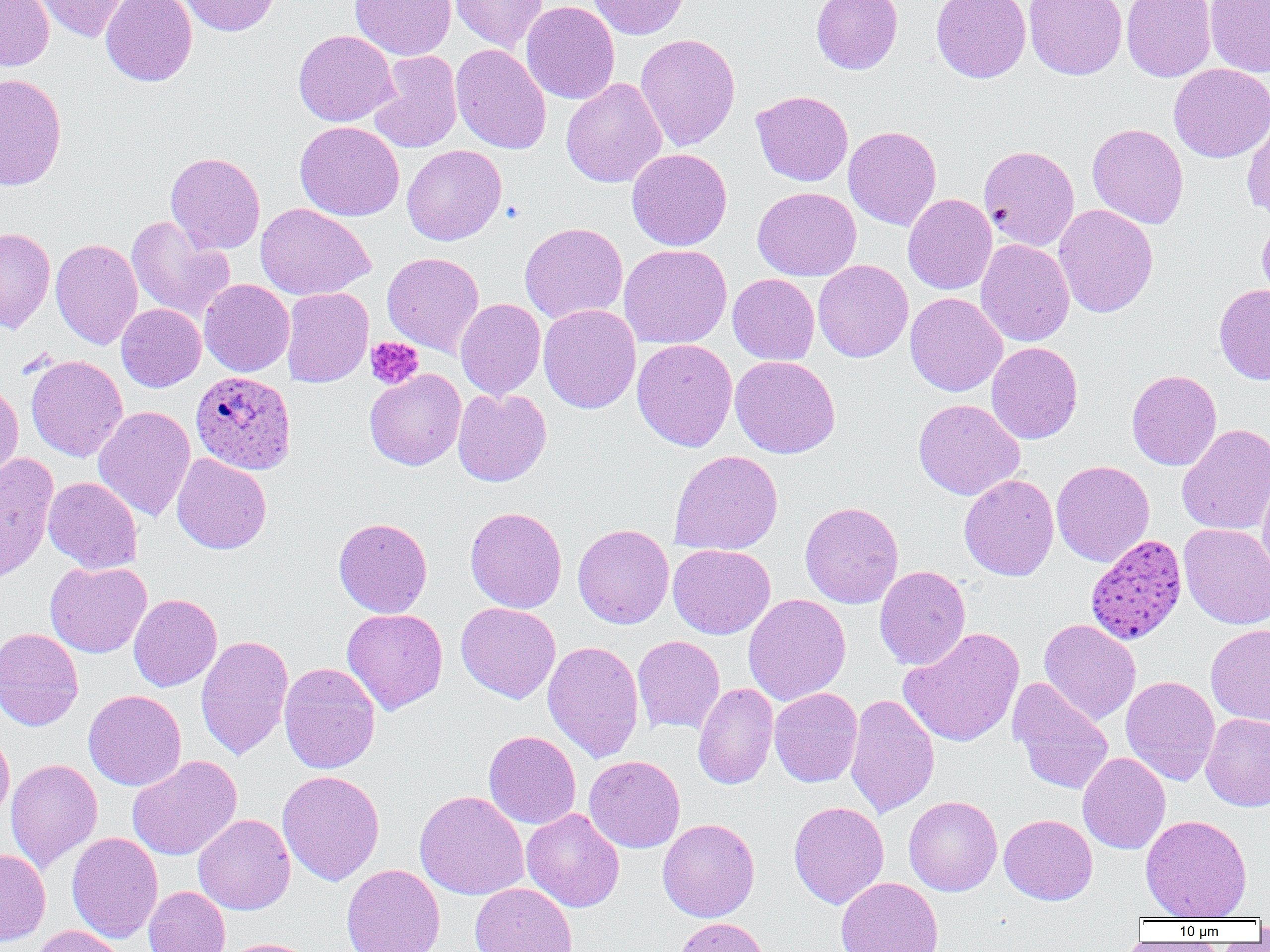

slide-level diagnosis = Plasmodium ovale
preparation = thin blood smear
Plasmodium ovale-infected red blood cell locations = approximate bounding boxes as [x1, y1, x2, y2] in pixels: [191, 370, 297, 474], [1085, 534, 1188, 645]
uninfected red blood cell locations = approximate bounding boxes as [x1, y1, x2, y2] in pixels: [0, 0, 54, 71], [32, 0, 131, 43], [101, 0, 197, 86], [177, 0, 280, 36], [349, 0, 457, 60], [449, 0, 547, 52], [588, 0, 690, 40], [811, 0, 902, 74], [931, 0, 1031, 82], [1023, 0, 1127, 80], [1121, 0, 1216, 82], [1204, 0, 1270, 77], [521, 1, 620, 105], [294, 30, 399, 126], [635, 33, 740, 151], [450, 43, 551, 154], [368, 51, 463, 153], [1168, 63, 1270, 163], [0, 73, 67, 191], [561, 78, 667, 188], [751, 90, 853, 187], [1241, 112, 1270, 221], [294, 121, 405, 221], [1087, 123, 1189, 229], [843, 126, 941, 230], [402, 145, 506, 245], [979, 145, 1080, 251], [626, 148, 732, 251], [165, 152, 265, 254], [752, 187, 861, 280], [903, 193, 997, 295], [255, 203, 375, 300], [1054, 204, 1158, 318], [126, 216, 235, 323], [1257, 216, 1270, 306], [519, 222, 628, 324], [0, 227, 56, 332], [50, 238, 143, 349], [975, 239, 1074, 347], [619, 243, 732, 349], [382, 252, 484, 356], [813, 260, 913, 362], [728, 273, 820, 365], [199, 278, 295, 376], [1214, 283, 1270, 385], [281, 287, 373, 388], [905, 292, 1008, 396], [455, 298, 546, 400], [116, 303, 205, 392], [538, 304, 640, 413], [632, 339, 737, 451], [986, 342, 1082, 443], [26, 354, 128, 461], [730, 355, 840, 459], [364, 369, 466, 470], [1126, 369, 1222, 470], [0, 382, 23, 487], [452, 388, 552, 487], [913, 398, 1025, 500], [93, 406, 196, 521], [1176, 423, 1270, 536], [669, 450, 784, 556], [0, 452, 59, 583], [172, 453, 272, 554], [1051, 460, 1155, 567], [959, 473, 1059, 581], [1257, 474, 1270, 579], [43, 477, 142, 573], [800, 501, 904, 608], [465, 506, 567, 613], [333, 517, 432, 618], [1179, 523, 1270, 629], [573, 524, 674, 629], [668, 544, 775, 639], [45, 561, 152, 658], [875, 565, 971, 670], [128, 594, 222, 691], [743, 594, 851, 705], [456, 602, 561, 703], [342, 608, 448, 714], [1039, 618, 1140, 726], [1206, 623, 1270, 726], [899, 627, 1025, 747], [0, 628, 84, 731], [196, 634, 294, 761], [632, 635, 725, 735], [543, 640, 644, 763], [279, 662, 380, 774], [1120, 675, 1220, 785], [1008, 678, 1114, 795], [692, 683, 779, 790], [769, 687, 863, 787], [83, 689, 186, 791], [845, 694, 940, 818], [1201, 712, 1270, 812], [0, 730, 14, 825], [483, 730, 581, 829], [1078, 752, 1170, 854], [127, 755, 242, 861], [584, 755, 685, 853], [5, 758, 103, 873], [277, 770, 385, 886], [415, 790, 529, 900], [903, 795, 1002, 896], [788, 801, 889, 909], [521, 808, 625, 912], [194, 814, 296, 915], [999, 814, 1097, 904], [1140, 814, 1252, 921], [657, 818, 760, 922], [67, 832, 163, 942], [0, 848, 51, 946], [341, 863, 445, 952], [836, 877, 943, 952], [470, 882, 577, 952], [144, 886, 230, 952], [675, 918, 769, 952], [29, 925, 128, 952], [219, 937, 319, 952]
field of view = one of a larger specimen
image size = 1270×952 pixels
platelet locations = approximate bounding boxes as [x1, y1, x2, y2] in pixels: [366, 337, 424, 389]
modality = optical microscopy
magnification = 1000x